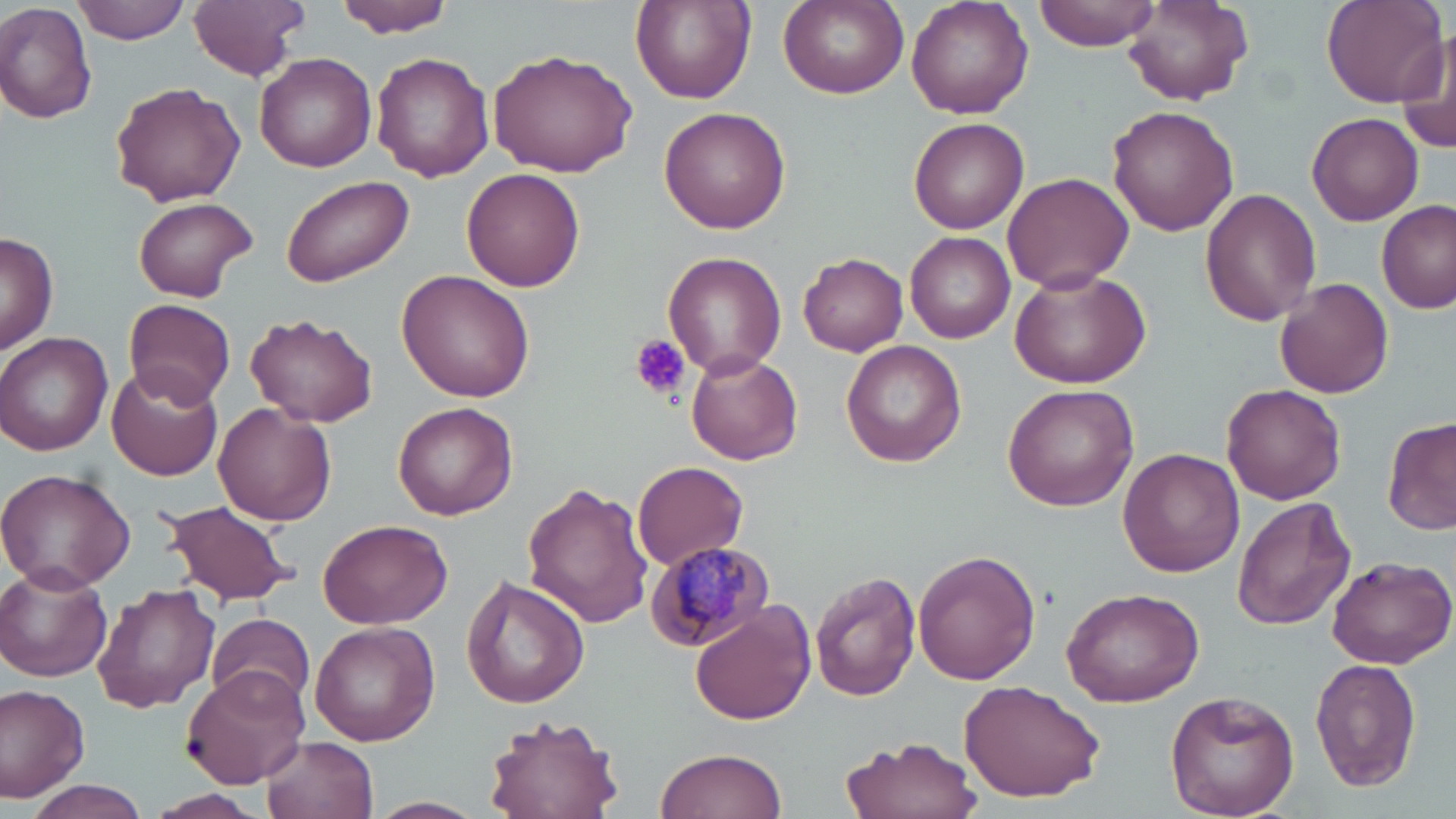

slide-level diagnosis = Plasmodium malariae
uninfected red blood cell locations = approximate bounding boxes as (x1, y1, x2, y2) in pixels: (71, 0, 192, 43), (332, 0, 458, 36), (630, 0, 757, 106), (906, 0, 1035, 117), (1036, 0, 1162, 51), (1321, 0, 1448, 108), (188, 1, 309, 79), (777, 1, 908, 100), (1123, 2, 1257, 107), (0, 4, 99, 125), (1395, 26, 1456, 157), (487, 49, 638, 177), (371, 52, 493, 182), (255, 54, 378, 171), (109, 81, 245, 207), (1107, 103, 1241, 235), (659, 107, 791, 233), (1306, 112, 1424, 225), (908, 117, 1029, 234), (463, 168, 585, 293), (1002, 171, 1134, 294), (282, 175, 414, 286), (1200, 188, 1322, 325), (132, 197, 256, 302), (1377, 201, 1455, 314), (1, 231, 59, 353), (905, 232, 1015, 343), (663, 250, 787, 376), (798, 252, 908, 356), (1007, 266, 1151, 388), (397, 269, 536, 401), (1275, 278, 1394, 398), (124, 298, 236, 408), (246, 313, 380, 427), (0, 332, 115, 457), (842, 341, 966, 467), (685, 350, 803, 466), (106, 366, 223, 481), (1221, 382, 1346, 504), (1003, 384, 1139, 512), (393, 401, 518, 520), (213, 404, 338, 527), (1383, 416, 1455, 538), (1117, 447, 1242, 577), (632, 461, 749, 571), (0, 468, 135, 592), (522, 482, 654, 628), (1233, 497, 1357, 630), (159, 499, 299, 606), (319, 518, 453, 629), (913, 550, 1041, 685), (1326, 556, 1456, 669), (0, 563, 114, 683), (810, 571, 920, 702), (461, 575, 590, 710), (91, 582, 222, 715), (1061, 586, 1204, 708), (688, 599, 817, 725), (206, 613, 316, 713), (309, 623, 439, 747), (1309, 657, 1421, 793), (183, 666, 309, 788), (957, 679, 1106, 802), (0, 685, 93, 801), (1163, 689, 1300, 818), (482, 712, 622, 819), (840, 734, 983, 819), (263, 735, 379, 819), (654, 746, 787, 819), (19, 778, 155, 819), (157, 791, 263, 816), (371, 796, 485, 818)
image size = 1456×819 pixels
magnification = 1000x
Plasmodium malariae-infected red blood cell locations = approximate bounding boxes as (x1, y1, x2, y2) in pixels: (644, 541, 777, 651)
modality = optical microscopy
field of view = one of a larger specimen
stain = May-Grünwald-Giemsa
preparation = thin blood film
platelet locations = approximate bounding boxes as (x1, y1, x2, y2) in pixels: (631, 334, 690, 401)